Comment on the morphology of the erythrocytes.
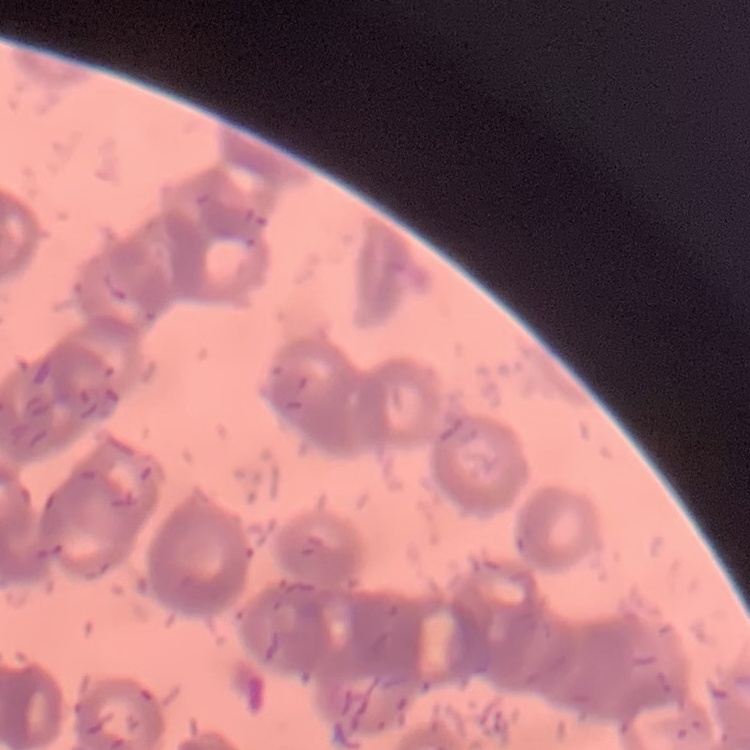

Rouleaux formation.

Summary:
  - Preparation: thin blood film
  - Image type: square crop of a larger photomicrograph
  - Stain: Field's or Giemsa